Assess the morphology of the erythrocytes.
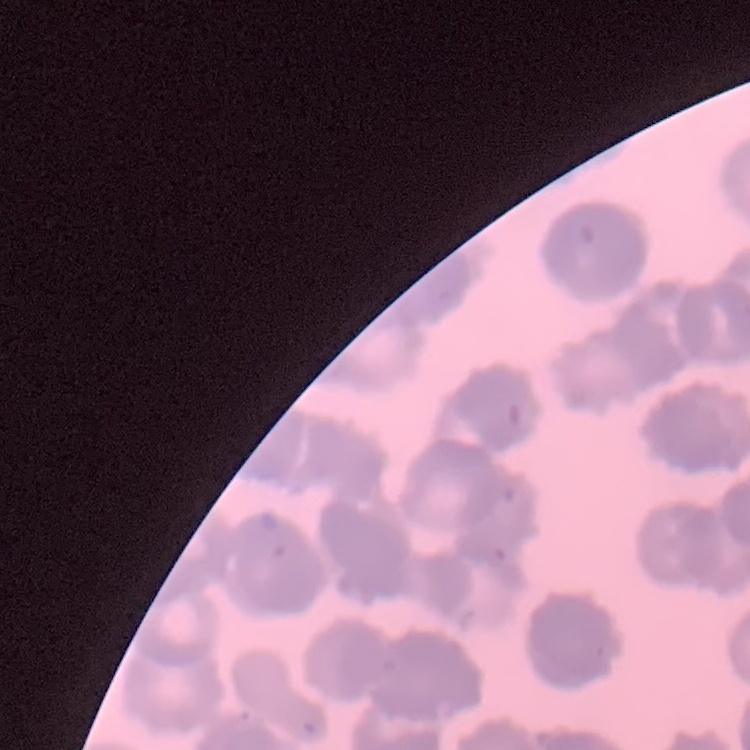
Rouleaux formation.

Thin blood film. Stained with either Field's or Giemsa. One tile cut from a larger photomicrograph.